Locate and identify every blood parasite.
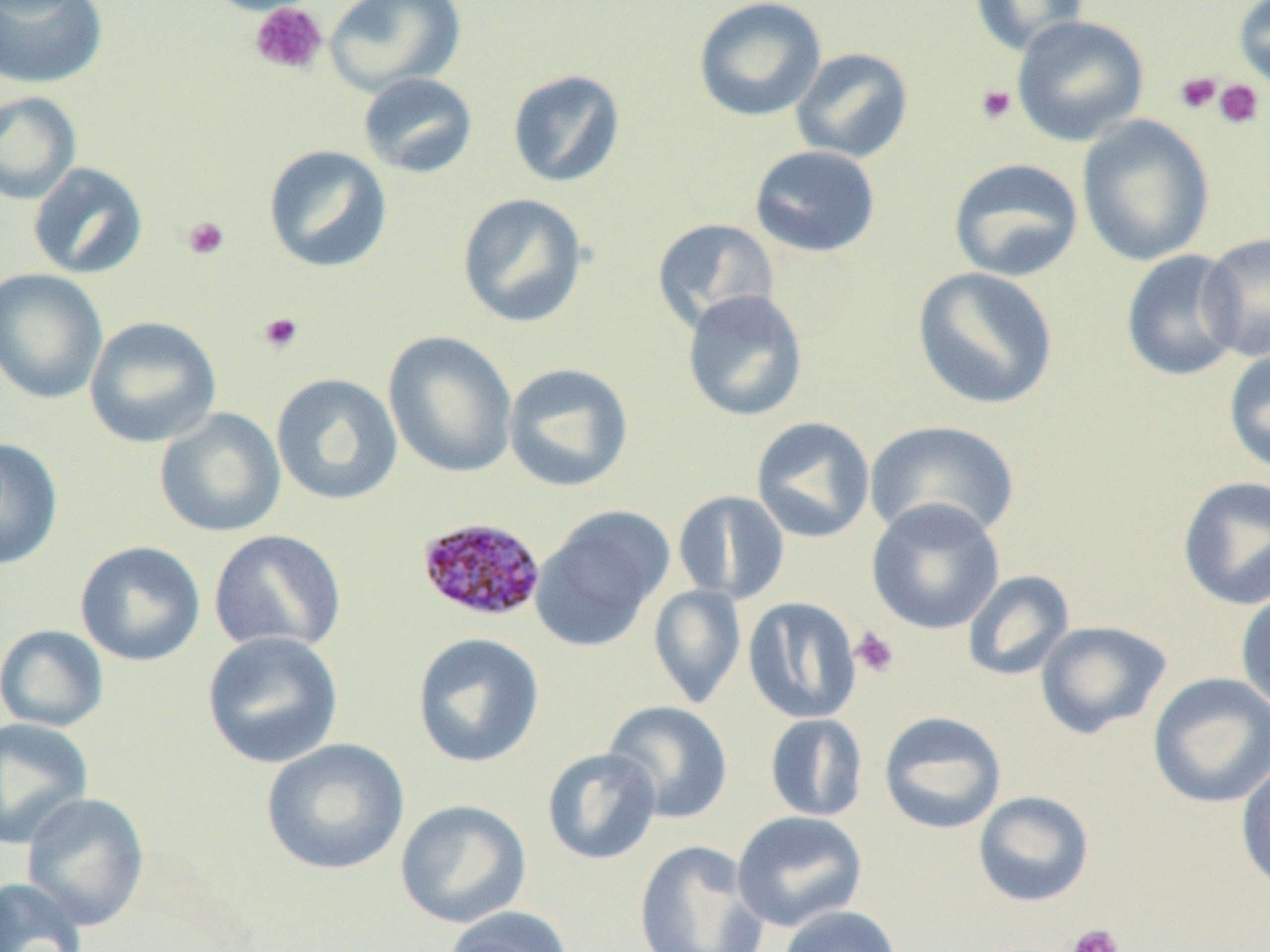

Approximate bounding boxes as [x1, y1, x2, y2] in pixels.
Plasmodium malariae-infected red blood cells: [417, 516, 546, 623].
No Plasmodium falciparum, Plasmodium ovale, Plasmodium vivax, Babesia divergens, or Trypanosoma brucei observed.

Summary:
  - Uninfected red blood cell locations: [199, 0, 322, 16], [324, 0, 466, 96], [693, 0, 827, 123], [968, 0, 1089, 56], [1233, 0, 1270, 95], [0, 1, 109, 90], [1012, 15, 1149, 146], [790, 47, 914, 163], [507, 68, 627, 188], [358, 72, 479, 179], [0, 90, 82, 205], [1076, 115, 1215, 266], [263, 144, 393, 274], [748, 145, 882, 258], [948, 157, 1084, 282], [27, 162, 148, 280], [456, 192, 590, 329], [651, 217, 780, 335], [1199, 232, 1270, 362], [1121, 249, 1245, 382], [912, 266, 1059, 411], [0, 268, 108, 405], [681, 289, 809, 422], [84, 315, 222, 449], [383, 330, 517, 478], [1223, 346, 1270, 475], [502, 362, 635, 493], [271, 372, 403, 506], [153, 407, 286, 538], [750, 416, 876, 543], [864, 420, 1020, 544], [0, 436, 64, 571], [1176, 475, 1270, 611], [673, 490, 790, 605], [866, 499, 1005, 635], [531, 506, 673, 651], [208, 529, 348, 655], [74, 541, 207, 667], [962, 569, 1075, 682], [648, 584, 746, 708], [1235, 587, 1270, 717], [743, 597, 862, 724], [1035, 620, 1172, 739], [0, 624, 109, 733], [201, 630, 345, 770], [412, 632, 545, 769], [1148, 672, 1270, 809], [602, 700, 733, 824], [878, 711, 1007, 834], [764, 713, 868, 821], [0, 717, 94, 849], [261, 737, 410, 875], [541, 747, 662, 866], [1235, 759, 1270, 895], [973, 790, 1095, 907], [20, 791, 150, 931], [395, 799, 532, 929], [732, 810, 868, 932], [633, 839, 770, 952], [0, 876, 90, 952], [443, 905, 574, 952], [778, 905, 903, 952]
  - Platelet locations: [249, 2, 328, 76], [1175, 72, 1221, 114], [1213, 79, 1264, 130], [976, 83, 1017, 125], [182, 216, 230, 260], [258, 312, 303, 353], [850, 626, 900, 678], [1066, 923, 1125, 952]
  - Slide-level diagnosis: Plasmodium malariae
  - Field of view: one of a larger specimen
  - Image size: 1270×952 pixels
  - Modality: optical microscopy
  - Magnification: 1000x
  - Preparation: thin blood smear